State the blood parasite species.
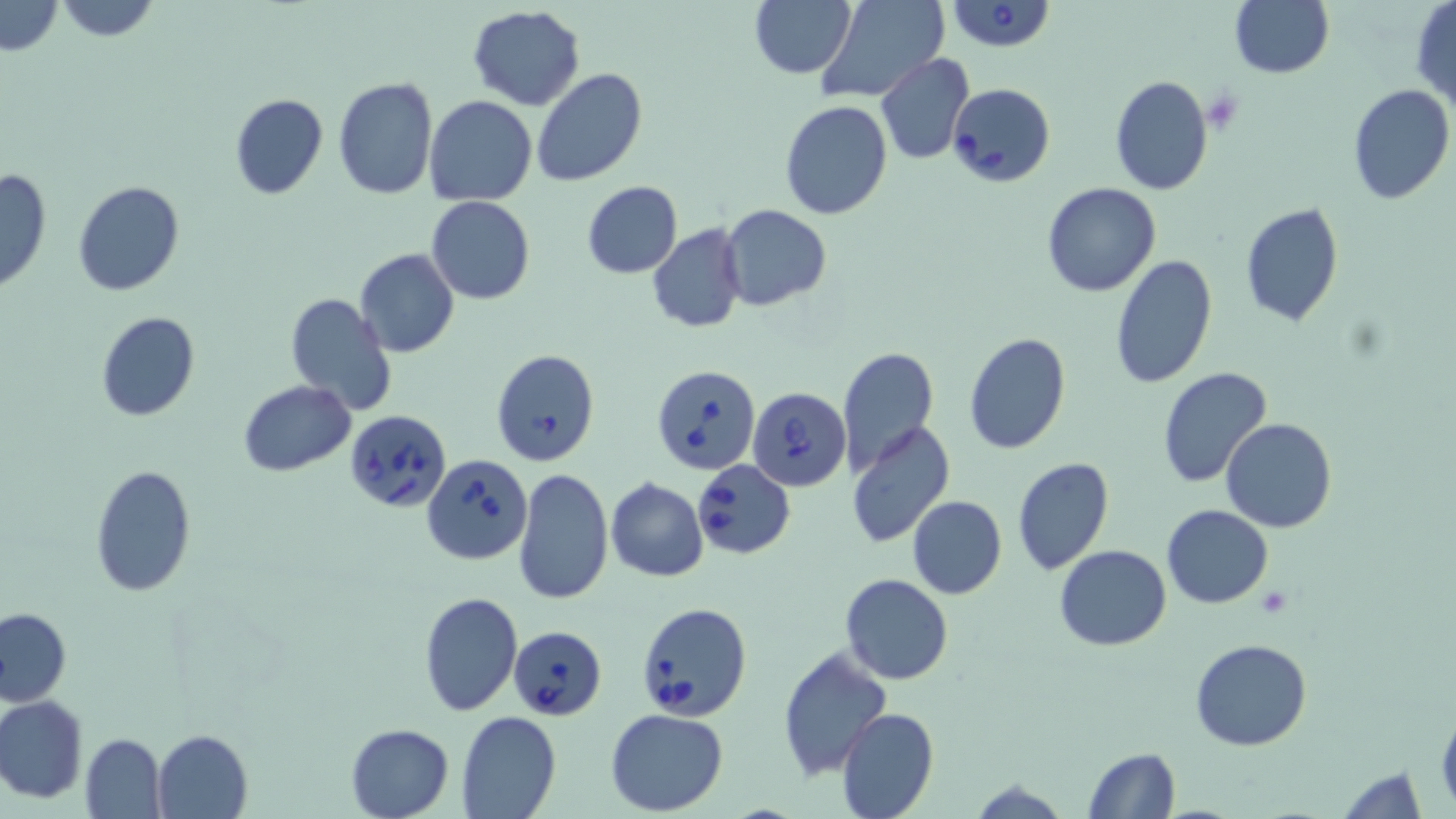

Babesia divergens.

{
  "modality": "optical microscopy",
  "field_of_view": "single",
  "image_size": "1456×819 pixels",
  "stain": "May-Grünwald-Giemsa",
  "babesia_divergens_infected_red_blood_cell_locations": "approximate bounding boxes as named x1/y1/x2/y2 corners in pixels: (x1=943, y1=0, x2=1057, y2=51), (x1=948, y1=82, x2=1056, y2=187), (x1=490, y1=348, x2=601, y2=468), (x1=651, y1=364, x2=760, y2=476), (x1=747, y1=386, x2=851, y2=491), (x1=343, y1=408, x2=450, y2=512), (x1=423, y1=453, x2=532, y2=564), (x1=691, y1=459, x2=795, y2=559), (x1=636, y1=602, x2=751, y2=721), (x1=508, y1=625, x2=606, y2=720)",
  "preparation": "thin blood smear",
  "uninfected_red_blood_cell_locations": "approximate bounding boxes as named x1/y1/x2/y2 corners in pixels: (x1=52, y1=0, x2=162, y2=42), (x1=750, y1=0, x2=855, y2=78), (x1=812, y1=0, x2=949, y2=103), (x1=1, y1=1, x2=64, y2=56), (x1=1229, y1=1, x2=1333, y2=78), (x1=1410, y1=2, x2=1456, y2=109), (x1=467, y1=6, x2=586, y2=110), (x1=875, y1=53, x2=973, y2=164), (x1=531, y1=67, x2=648, y2=186), (x1=1109, y1=74, x2=1214, y2=195), (x1=332, y1=77, x2=438, y2=201), (x1=1346, y1=84, x2=1456, y2=205), (x1=228, y1=93, x2=329, y2=200), (x1=425, y1=95, x2=537, y2=205), (x1=779, y1=99, x2=892, y2=220), (x1=0, y1=168, x2=52, y2=295), (x1=72, y1=179, x2=186, y2=297), (x1=582, y1=181, x2=683, y2=278), (x1=1041, y1=181, x2=1161, y2=296), (x1=426, y1=197, x2=534, y2=304), (x1=1239, y1=203, x2=1344, y2=326), (x1=719, y1=205, x2=831, y2=310), (x1=647, y1=222, x2=747, y2=333), (x1=355, y1=249, x2=458, y2=360), (x1=1108, y1=253, x2=1219, y2=389), (x1=288, y1=293, x2=397, y2=415), (x1=97, y1=311, x2=200, y2=422), (x1=963, y1=333, x2=1072, y2=455), (x1=836, y1=346, x2=939, y2=475), (x1=1156, y1=366, x2=1274, y2=490), (x1=238, y1=379, x2=356, y2=476), (x1=1221, y1=418, x2=1337, y2=533), (x1=846, y1=421, x2=957, y2=551), (x1=1012, y1=457, x2=1113, y2=575), (x1=88, y1=463, x2=197, y2=597), (x1=513, y1=467, x2=614, y2=606), (x1=606, y1=477, x2=708, y2=581), (x1=907, y1=496, x2=1007, y2=599), (x1=1162, y1=504, x2=1273, y2=608), (x1=1054, y1=544, x2=1172, y2=651), (x1=840, y1=574, x2=953, y2=685), (x1=418, y1=591, x2=522, y2=717), (x1=0, y1=608, x2=72, y2=706), (x1=1191, y1=638, x2=1311, y2=751), (x1=776, y1=645, x2=890, y2=781), (x1=1, y1=695, x2=88, y2=803), (x1=1436, y1=705, x2=1456, y2=810), (x1=836, y1=707, x2=939, y2=819), (x1=606, y1=708, x2=729, y2=815), (x1=457, y1=711, x2=561, y2=819), (x1=345, y1=723, x2=453, y2=818), (x1=152, y1=729, x2=252, y2=817), (x1=79, y1=734, x2=167, y2=819), (x1=1082, y1=747, x2=1181, y2=819), (x1=1334, y1=765, x2=1428, y2=819)",
  "magnification": "1000x"
}